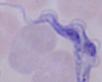

identification: trypanosome
magnification: 1000x
modality: photomicrograph